Assess this cell for malaria.
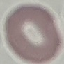

It is uninfected.

preparation = thin smear
stain = Giemsa
image type = automatically extracted cell patch, resized to 64 × 64 pixels
capture = smartphone through the microscope eyepiece